Locate every blood parasite and identify its species.
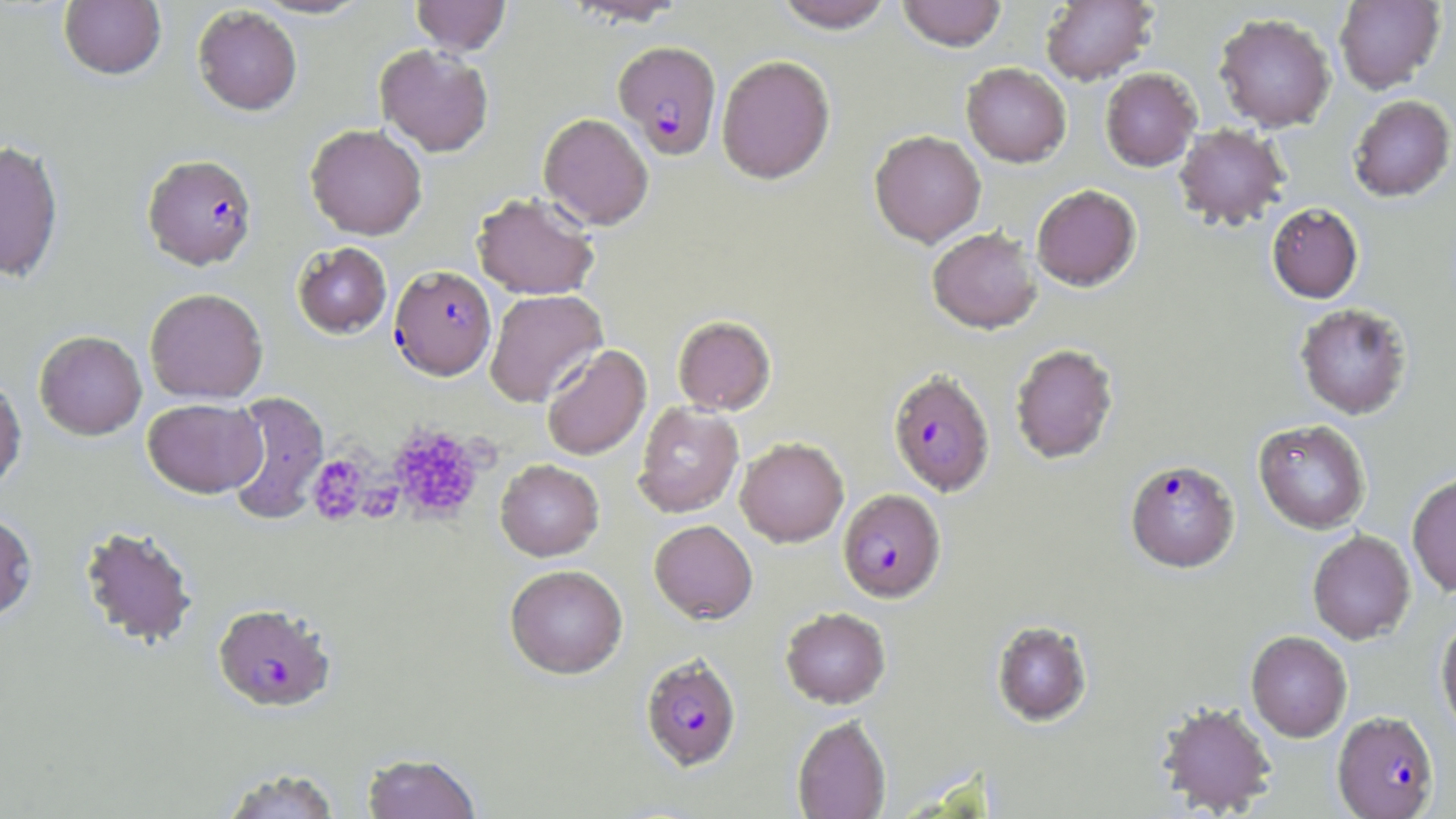

Approximate bounding boxes as (x1,y1)-(x2,y2) corner pairs in pixels.
Plasmodium falciparum-infected red blood cells: (613,41)-(722,160), (142,154)-(257,269), (389,265)-(496,380), (888,369)-(995,496), (1125,459)-(1239,573), (838,489)-(946,603), (213,603)-(336,712), (640,654)-(742,771), (1332,710)-(1439,818).
No Plasmodium ovale, Plasmodium malariae, Plasmodium vivax, Babesia divergens, or Trypanosoma brucei observed.

Summary:
  - Uninfected red blood cell locations: (251,0)-(374,20), (411,0)-(511,56), (563,0)-(688,26), (773,0)-(896,33), (896,0)-(1007,51), (1040,0)-(1158,85), (1334,0)-(1445,93), (59,1)-(166,80), (192,5)-(303,115), (1214,12)-(1336,132), (375,44)-(494,157), (716,54)-(836,184), (961,63)-(1071,167), (1100,67)-(1201,172), (1348,95)-(1455,202), (538,113)-(654,229), (305,123)-(427,240), (1173,124)-(1290,230), (869,130)-(986,247), (0,140)-(64,282), (1031,184)-(1141,291), (472,192)-(600,300), (1266,203)-(1364,304), (927,227)-(1042,334), (292,242)-(391,338), (144,287)-(268,403), (485,289)-(607,407), (1294,303)-(1413,419), (672,315)-(776,415), (34,331)-(147,440), (1010,343)-(1119,464), (541,344)-(651,461), (0,374)-(26,492), (224,391)-(329,525), (142,398)-(266,497), (633,402)-(744,518), (1254,420)-(1371,534), (735,437)-(849,547), (495,459)-(604,561), (1407,473)-(1456,596), (0,511)-(38,622), (649,520)-(758,624), (79,525)-(199,650), (1307,530)-(1416,645), (504,564)-(628,679), (780,607)-(891,708), (1436,615)-(1456,739), (992,620)-(1092,726), (1246,630)-(1352,742), (1155,701)-(1277,816), (792,715)-(890,819), (362,753)-(482,819), (219,767)-(342,818)
  - Platelet locations: (387,423)-(486,523), (307,454)-(369,525), (358,481)-(403,523)
  - Slide-level diagnosis: Plasmodium falciparum
  - Preparation: thin blood smear
  - Stain: May-Grünwald-Giemsa
  - Magnification: 1000x
  - Field of view: one of a larger specimen
  - Modality: optical microscopy
  - Image size: 1456×819 pixels